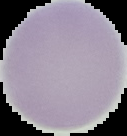

Summary:
  - Image type: cell region segmented out of the field of view; surrounding area masked to black
  - Image size: 127×136 pixels
  - Preparation: thin blood film
  - Malaria status: uninfected